Name the blood parasite species.
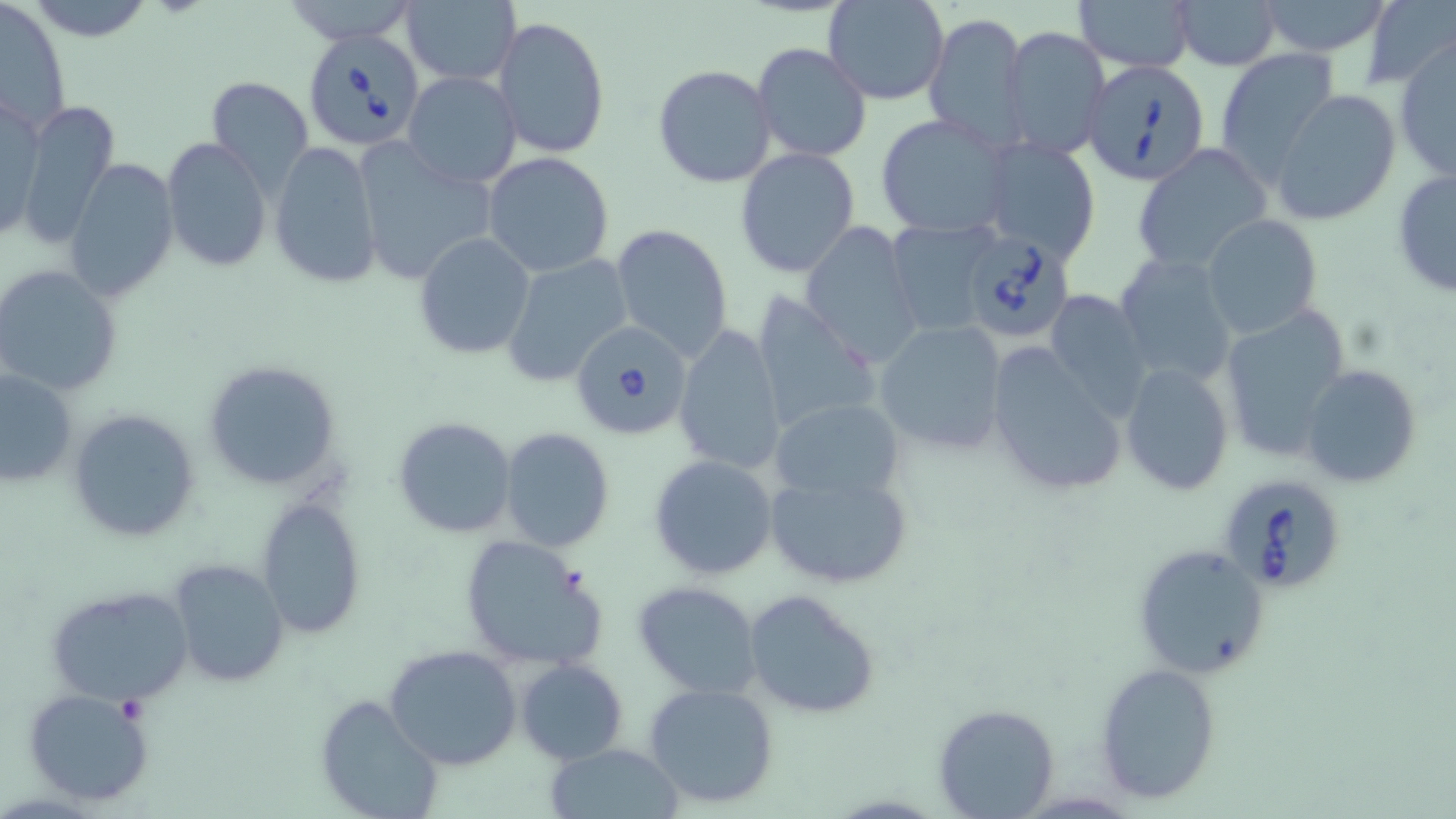

Babesia divergens.

Approximate bounding boxes as [x1, y1, x2, y2] in pixels. Platelet locations: [116, 698, 148, 726]. Babesia divergens-infected red blood cell locations: [303, 28, 424, 151], [1083, 59, 1212, 186], [957, 229, 1080, 345], [566, 319, 694, 443], [1215, 472, 1349, 596]. Uninfected red blood cell locations: [2, 0, 72, 134], [22, 0, 157, 44], [282, 0, 419, 46], [825, 0, 948, 104], [1072, 0, 1197, 73], [1256, 0, 1395, 57], [1361, 0, 1455, 89], [1172, 1, 1283, 71], [402, 2, 520, 86], [924, 12, 1029, 146], [494, 15, 610, 160], [999, 26, 1110, 159], [1394, 38, 1456, 182], [751, 42, 872, 164], [1217, 48, 1340, 173], [653, 64, 776, 187], [403, 70, 521, 190], [206, 76, 313, 195], [1272, 90, 1402, 227], [1, 91, 44, 242], [12, 98, 120, 250], [877, 114, 1012, 238], [161, 137, 270, 272], [979, 137, 1102, 266], [268, 139, 384, 289], [351, 141, 499, 286], [1131, 143, 1272, 273], [734, 147, 861, 279], [482, 152, 616, 278], [64, 159, 179, 301], [1391, 168, 1456, 300], [1201, 215, 1321, 337], [887, 219, 1000, 335], [800, 221, 925, 369], [611, 224, 734, 362], [414, 231, 536, 361], [1114, 252, 1237, 384], [502, 255, 634, 385], [1, 265, 122, 396], [747, 290, 882, 437], [1042, 290, 1154, 419], [1216, 302, 1355, 459], [873, 318, 1008, 455], [674, 324, 787, 477], [983, 341, 1131, 500], [202, 358, 342, 490], [1119, 362, 1233, 497], [1300, 364, 1423, 488], [1, 368, 77, 489], [771, 397, 907, 505], [68, 408, 200, 543], [392, 415, 519, 539], [500, 427, 615, 551], [649, 454, 779, 580], [764, 468, 917, 590], [256, 496, 367, 639], [458, 534, 605, 672], [1132, 543, 1269, 679], [167, 559, 289, 686], [632, 580, 765, 700], [45, 584, 190, 704], [742, 587, 880, 718], [385, 644, 522, 771], [515, 658, 628, 764], [1095, 663, 1222, 805], [644, 682, 780, 809], [23, 686, 156, 808], [315, 692, 444, 819], [934, 703, 1060, 818], [544, 742, 684, 818]. Image is 1456×819 pixels. May-Grünwald-Giemsa-stained preparation. 1000x magnification. Thin blood smear. One field of a larger specimen. Light microscopy.